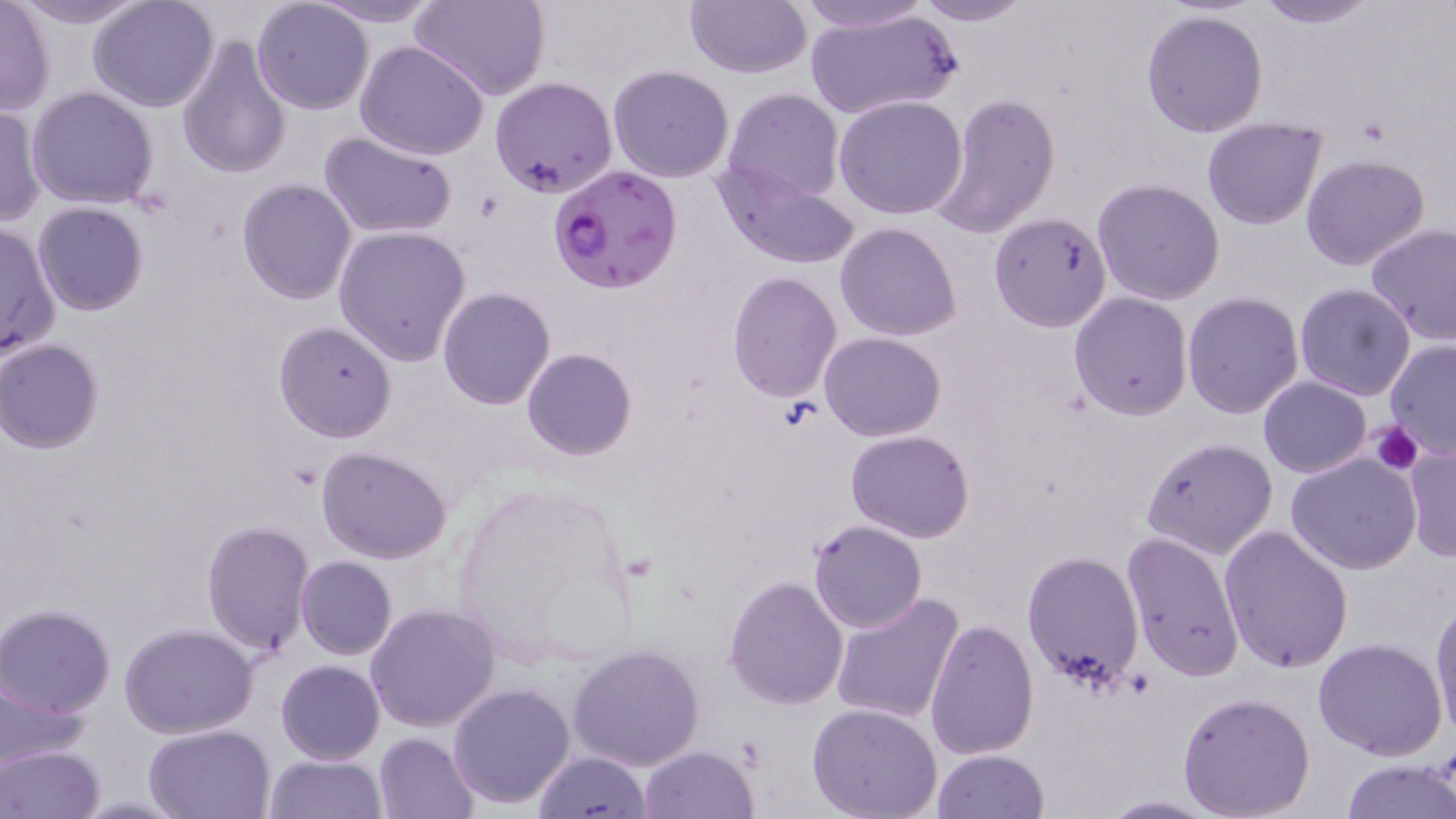
Summary:
  - Coordinate format: approximate bounding boxes as named x1/y1/x2/y2 corners in pixels
  - Plasmodium falciparum-infected red blood cell locations: (x1=548, y1=163, x2=681, y2=294)
  - Platelet locations: (x1=1370, y1=420, x2=1423, y2=474)
  - Uninfected red blood cell locations: (x1=11, y1=0, x2=152, y2=28), (x1=87, y1=0, x2=219, y2=112), (x1=309, y1=0, x2=444, y2=27), (x1=414, y1=0, x2=550, y2=103), (x1=788, y1=0, x2=937, y2=34), (x1=908, y1=0, x2=1037, y2=25), (x1=1250, y1=0, x2=1382, y2=27), (x1=0, y1=1, x2=54, y2=116), (x1=684, y1=1, x2=812, y2=79), (x1=252, y1=2, x2=374, y2=115), (x1=802, y1=7, x2=963, y2=120), (x1=1139, y1=7, x2=1268, y2=140), (x1=176, y1=35, x2=291, y2=179), (x1=355, y1=39, x2=491, y2=162), (x1=607, y1=64, x2=735, y2=183), (x1=489, y1=76, x2=618, y2=199), (x1=28, y1=85, x2=158, y2=208), (x1=721, y1=88, x2=843, y2=204), (x1=929, y1=92, x2=1061, y2=238), (x1=833, y1=95, x2=968, y2=220), (x1=0, y1=103, x2=45, y2=226), (x1=1201, y1=117, x2=1328, y2=230), (x1=319, y1=129, x2=458, y2=238), (x1=1300, y1=153, x2=1431, y2=270), (x1=716, y1=161, x2=863, y2=271), (x1=1092, y1=177, x2=1225, y2=305), (x1=236, y1=178, x2=356, y2=304), (x1=32, y1=202, x2=149, y2=316), (x1=989, y1=212, x2=1114, y2=332), (x1=0, y1=220, x2=61, y2=363), (x1=835, y1=222, x2=961, y2=340), (x1=1365, y1=223, x2=1456, y2=345), (x1=331, y1=225, x2=474, y2=366), (x1=727, y1=272, x2=841, y2=401), (x1=1295, y1=283, x2=1417, y2=401), (x1=437, y1=287, x2=556, y2=409), (x1=1182, y1=291, x2=1304, y2=419), (x1=1069, y1=293, x2=1193, y2=419), (x1=272, y1=321, x2=398, y2=443), (x1=818, y1=332, x2=946, y2=440), (x1=2, y1=339, x2=107, y2=453), (x1=1384, y1=340, x2=1456, y2=458), (x1=521, y1=348, x2=636, y2=461), (x1=1258, y1=377, x2=1370, y2=478), (x1=846, y1=430, x2=976, y2=542), (x1=1141, y1=436, x2=1277, y2=561), (x1=317, y1=446, x2=452, y2=564), (x1=1403, y1=446, x2=1456, y2=562), (x1=1287, y1=452, x2=1421, y2=574), (x1=808, y1=519, x2=928, y2=634), (x1=201, y1=521, x2=315, y2=658), (x1=1219, y1=524, x2=1352, y2=672), (x1=1121, y1=530, x2=1245, y2=681), (x1=814, y1=547, x2=942, y2=690), (x1=1021, y1=549, x2=1143, y2=689), (x1=295, y1=555, x2=397, y2=660), (x1=723, y1=575, x2=849, y2=708), (x1=830, y1=590, x2=965, y2=724), (x1=1428, y1=596, x2=1456, y2=743), (x1=365, y1=603, x2=500, y2=733), (x1=1, y1=604, x2=117, y2=717), (x1=923, y1=618, x2=1039, y2=761), (x1=118, y1=623, x2=258, y2=737), (x1=1313, y1=637, x2=1449, y2=761), (x1=568, y1=642, x2=704, y2=771), (x1=277, y1=659, x2=384, y2=765), (x1=0, y1=673, x2=90, y2=767), (x1=448, y1=682, x2=577, y2=809), (x1=1178, y1=692, x2=1315, y2=819), (x1=806, y1=703, x2=945, y2=819), (x1=143, y1=723, x2=274, y2=817), (x1=372, y1=732, x2=477, y2=819), (x1=1, y1=744, x2=105, y2=819), (x1=638, y1=744, x2=760, y2=819), (x1=931, y1=748, x2=1050, y2=818), (x1=535, y1=751, x2=652, y2=819), (x1=264, y1=752, x2=385, y2=819), (x1=1337, y1=758, x2=1456, y2=819), (x1=1094, y1=795, x2=1228, y2=818)
  - Slide-level diagnosis: Plasmodium falciparum
  - Magnification: 1000x
  - Stain: May-Grünwald-Giemsa
  - Modality: light microscopy
  - Preparation: thin blood smear
  - Image size: 1456×819 pixels
  - Field of view: one of a larger specimen